Assess this cell for malaria.
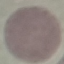

It is uninfected.

image type = automatically extracted cell patch, resized to 64 × 64 pixels
preparation = thin blood smear
capture = smartphone through the microscope eyepiece
stain = Giemsa